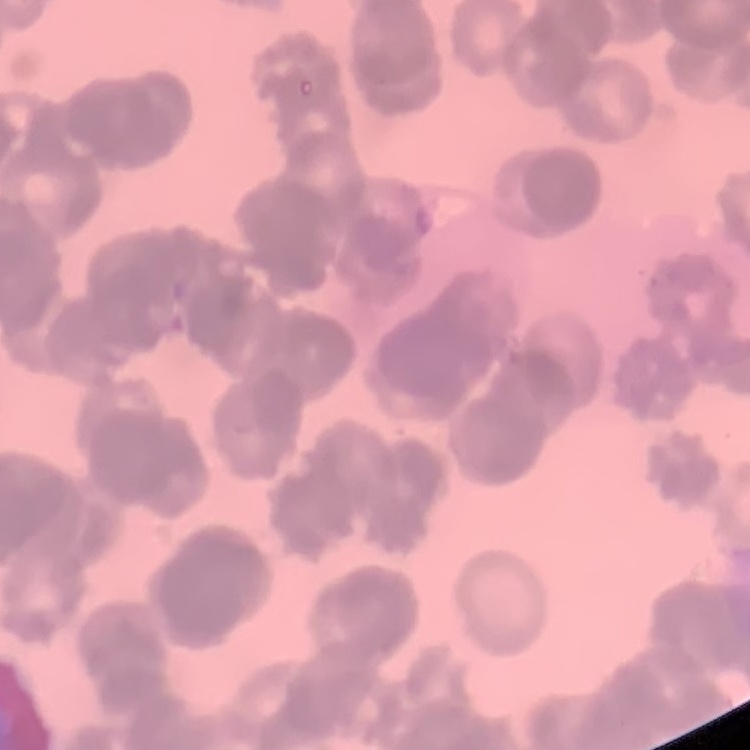

{
  "erythrocyte_morphology": "rouleaux formation",
  "image_type": "one tile cut from a larger photomicrograph",
  "stain": "Field's or Giemsa",
  "preparation": "thin peripheral smear"
}